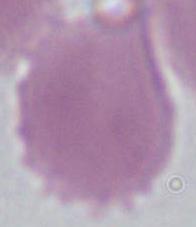

magnification = 1000x
modality = micrograph
identification = red blood cell